Classify this cell by malaria status.
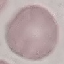
Uninfected.

Acquired by smartphone through the microscope eyepiece. Thin blood film. Giemsa-stained preparation. Automatically extracted cell patch, resized to 64 × 64 pixels.